Outline each uninfected red blood cell.
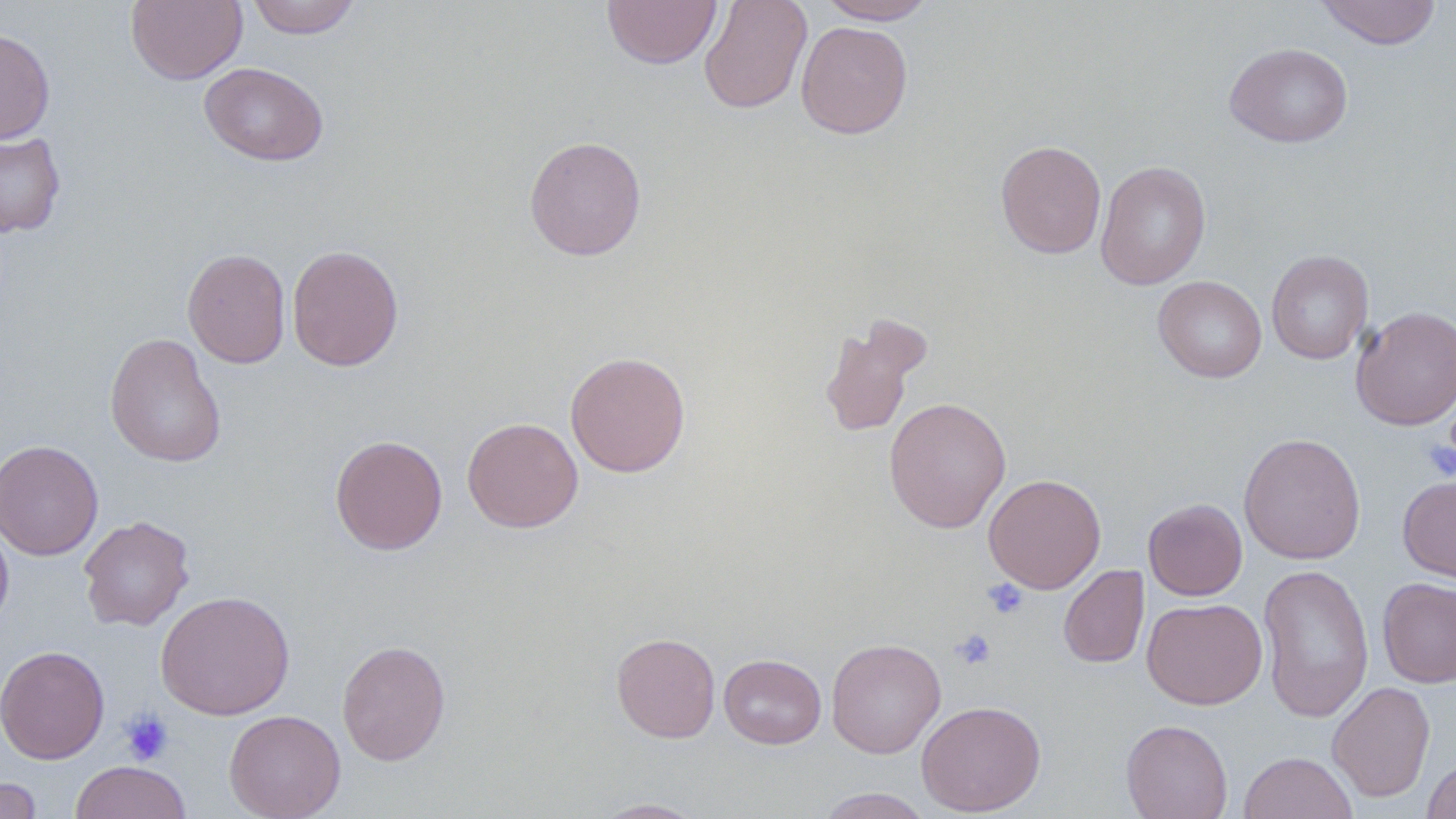

Approximate bounding boxes as [x1, y1, x2, y2] in pixels.
Uninfected red blood cells: [126, 0, 247, 85], [246, 0, 361, 38], [602, 0, 722, 69], [699, 0, 812, 114], [818, 0, 938, 24], [1315, 0, 1442, 49], [795, 21, 913, 139], [0, 27, 55, 145], [1224, 42, 1353, 148], [200, 62, 328, 166], [0, 130, 66, 238], [524, 135, 647, 260], [996, 139, 1106, 259], [1096, 160, 1211, 290], [286, 244, 404, 371], [182, 248, 291, 368], [1266, 250, 1374, 364], [1153, 276, 1267, 382], [1351, 306, 1456, 430], [818, 315, 930, 438], [105, 332, 227, 468], [565, 351, 691, 477], [883, 396, 1011, 533], [461, 417, 583, 533], [1238, 432, 1366, 564], [330, 434, 448, 555], [0, 440, 104, 561], [983, 473, 1106, 593], [1398, 474, 1456, 587], [1143, 498, 1247, 600], [0, 515, 14, 632], [78, 515, 195, 631], [1258, 563, 1374, 722], [1058, 565, 1149, 668], [1377, 577, 1456, 688], [155, 590, 295, 720], [1142, 598, 1267, 709], [611, 632, 721, 743], [826, 638, 946, 759], [336, 640, 450, 765], [0, 645, 110, 764], [719, 653, 826, 749], [1327, 681, 1435, 801], [916, 700, 1046, 816], [224, 709, 346, 819], [1121, 719, 1233, 819], [1238, 751, 1358, 818], [1422, 757, 1456, 818], [69, 760, 193, 819], [0, 777, 43, 818], [816, 787, 934, 818], [591, 798, 708, 818].

slide-level diagnosis = negative for blood parasites
preparation = thin blood smear
stain = May-Grünwald-Giemsa
image size = 1456×819 pixels
magnification = 1000x
modality = optical microscopy
platelet locations = approximate bounding boxes as [x1, y1, x2, y2] in pixels: [1421, 438, 1455, 481], [982, 578, 1029, 619], [950, 628, 996, 670], [119, 709, 175, 766]
field of view = one of a larger specimen